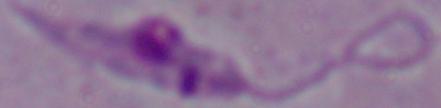

Summary:
  - Modality: photomicrograph
  - Identification: Leishmania
  - Magnification: 1000x